State which cell type is depicted.
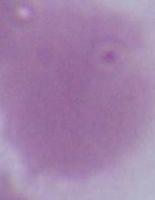

This is an erythrocyte.

Micrograph. Captured at 1000x magnification.